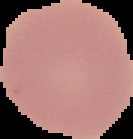

{
  "malaria_status": "uninfected",
  "preparation": "thin blood smear",
  "image_size": "133×139 pixels",
  "image_type": "cell region segmented out of the field of view; surrounding area masked to black"
}